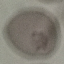

malaria_status: uninfected
image_type: automatically extracted cell patch, resized to 64 × 64 pixels
preparation: thin smear
capture: smartphone camera at the microscope eyepiece
stain: Giemsa